Report the malaria status of this cell.
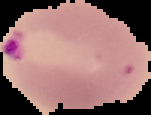
Parasitized.

image size = 151×115 pixels
image type = segmented cell region on a black background
preparation = thin blood smear